Name the blood parasite species.
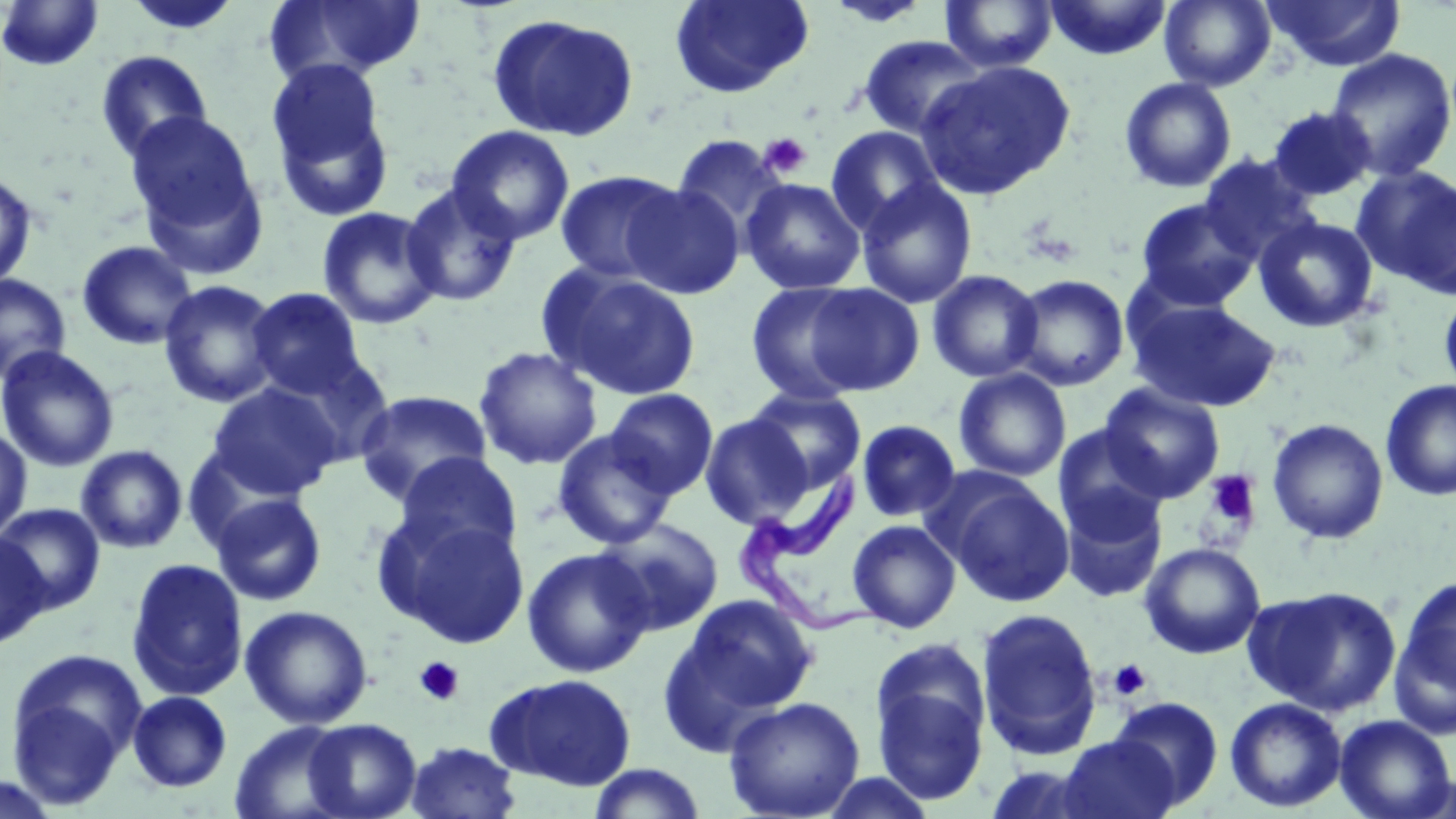
Trypanosoma brucei.

Summary:
  - Coordinate format: approximate bounding boxes as named x1/y1/x2/y2 corners in pixels
  - Platelet locations: (x1=758, y1=132, x2=811, y2=180), (x1=1203, y1=470, x2=1262, y2=533), (x1=414, y1=657, x2=465, y2=706), (x1=1107, y1=659, x2=1152, y2=701)
  - Trypanosoma brucei locations: (x1=729, y1=469, x2=887, y2=638)
  - Uninfected red blood cell locations: (x1=124, y1=0, x2=242, y2=37), (x1=264, y1=0, x2=426, y2=86), (x1=669, y1=0, x2=814, y2=99), (x1=822, y1=0, x2=935, y2=27), (x1=1044, y1=0, x2=1173, y2=61), (x1=1159, y1=0, x2=1276, y2=92), (x1=1263, y1=0, x2=1405, y2=72), (x1=1, y1=1, x2=104, y2=71), (x1=939, y1=1, x2=1059, y2=73), (x1=486, y1=12, x2=641, y2=143), (x1=856, y1=34, x2=988, y2=141), (x1=1325, y1=48, x2=1456, y2=182), (x1=95, y1=50, x2=214, y2=164), (x1=917, y1=59, x2=1077, y2=200), (x1=264, y1=64, x2=397, y2=218), (x1=1119, y1=77, x2=1237, y2=193), (x1=1267, y1=105, x2=1377, y2=201), (x1=125, y1=110, x2=266, y2=263), (x1=446, y1=125, x2=576, y2=245), (x1=825, y1=125, x2=945, y2=236), (x1=670, y1=134, x2=789, y2=243), (x1=1197, y1=152, x2=1320, y2=264), (x1=1353, y1=165, x2=1456, y2=296), (x1=554, y1=169, x2=686, y2=284), (x1=0, y1=170, x2=38, y2=290), (x1=856, y1=177, x2=978, y2=309), (x1=740, y1=178, x2=865, y2=295), (x1=400, y1=183, x2=524, y2=308), (x1=622, y1=183, x2=745, y2=299), (x1=1133, y1=197, x2=1261, y2=311), (x1=317, y1=206, x2=444, y2=329), (x1=1253, y1=216, x2=1380, y2=333), (x1=77, y1=240, x2=198, y2=350), (x1=540, y1=265, x2=703, y2=400), (x1=926, y1=269, x2=1045, y2=383), (x1=0, y1=273, x2=71, y2=385), (x1=1008, y1=274, x2=1130, y2=391), (x1=159, y1=280, x2=282, y2=408), (x1=746, y1=281, x2=869, y2=405), (x1=803, y1=283, x2=925, y2=396), (x1=246, y1=287, x2=367, y2=399), (x1=1439, y1=288, x2=1456, y2=401), (x1=1126, y1=295, x2=1282, y2=413), (x1=0, y1=345, x2=120, y2=473), (x1=473, y1=346, x2=603, y2=471), (x1=269, y1=354, x2=397, y2=469), (x1=954, y1=369, x2=1072, y2=481), (x1=1379, y1=379, x2=1456, y2=501), (x1=207, y1=382, x2=342, y2=501), (x1=1099, y1=384, x2=1226, y2=503), (x1=746, y1=387, x2=867, y2=493), (x1=605, y1=388, x2=719, y2=499), (x1=354, y1=390, x2=493, y2=506), (x1=700, y1=413, x2=812, y2=529), (x1=1266, y1=418, x2=1390, y2=543), (x1=855, y1=419, x2=961, y2=523), (x1=1053, y1=423, x2=1169, y2=539), (x1=0, y1=425, x2=32, y2=541), (x1=552, y1=429, x2=677, y2=550), (x1=76, y1=445, x2=188, y2=554), (x1=394, y1=452, x2=523, y2=563), (x1=939, y1=475, x2=1076, y2=607), (x1=1059, y1=488, x2=1168, y2=604), (x1=210, y1=492, x2=327, y2=607), (x1=0, y1=504, x2=105, y2=615), (x1=379, y1=510, x2=532, y2=647), (x1=594, y1=518, x2=724, y2=637), (x1=847, y1=519, x2=961, y2=633), (x1=0, y1=533, x2=50, y2=650), (x1=1139, y1=542, x2=1266, y2=660), (x1=521, y1=547, x2=654, y2=678), (x1=125, y1=558, x2=249, y2=701), (x1=1392, y1=576, x2=1456, y2=725), (x1=1246, y1=584, x2=1403, y2=716), (x1=666, y1=593, x2=818, y2=734), (x1=239, y1=605, x2=374, y2=729), (x1=976, y1=608, x2=1103, y2=761), (x1=869, y1=640, x2=993, y2=805), (x1=5, y1=648, x2=146, y2=804), (x1=485, y1=673, x2=636, y2=792), (x1=127, y1=690, x2=232, y2=793), (x1=724, y1=696, x2=866, y2=818), (x1=1109, y1=696, x2=1225, y2=810), (x1=1224, y1=697, x2=1347, y2=813), (x1=1334, y1=714, x2=1455, y2=819), (x1=300, y1=718, x2=422, y2=819), (x1=229, y1=720, x2=355, y2=819), (x1=1054, y1=735, x2=1182, y2=819), (x1=405, y1=742, x2=522, y2=818), (x1=587, y1=763, x2=708, y2=819), (x1=815, y1=771, x2=939, y2=818), (x1=0, y1=774, x2=61, y2=818)
  - Modality: light microscopy
  - Magnification: 1000x
  - Field of view: single
  - Image size: 1456×819 pixels
  - Preparation: thin blood smear
  - Stain: May-Grünwald-Giemsa